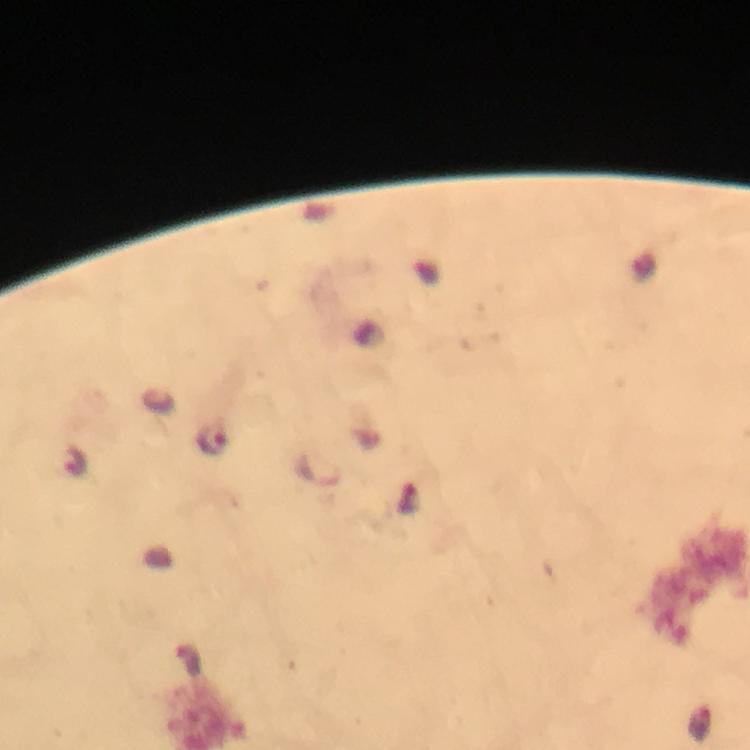
{
  "capture": "smartphone mounted on the microscope",
  "stain": "Giemsa",
  "cropped_from": "one field of view",
  "preparation": "thick blood smear",
  "plasmodium_parasite_locations": "approximate centers as {x, y} in pixels: {211, 440}, {318, 471}",
  "magnification": "100x",
  "context": "from a diagnostic examination for malaria",
  "image_size": "750×750 pixels",
  "immersion_oil": "applied"
}